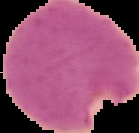

preparation = thin blood smear
image type = segmented cell region on a black background
image size = 139×133 pixels
result = malaria parasites identified